Name the parasite shown.
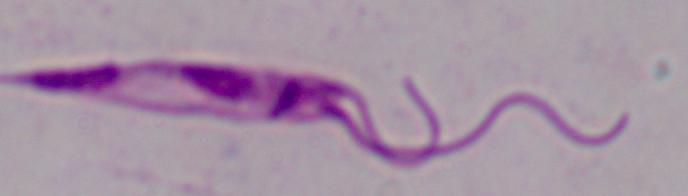
This is Leishmania.

modality = micrograph
magnification = 1000x